Give the preparation type.
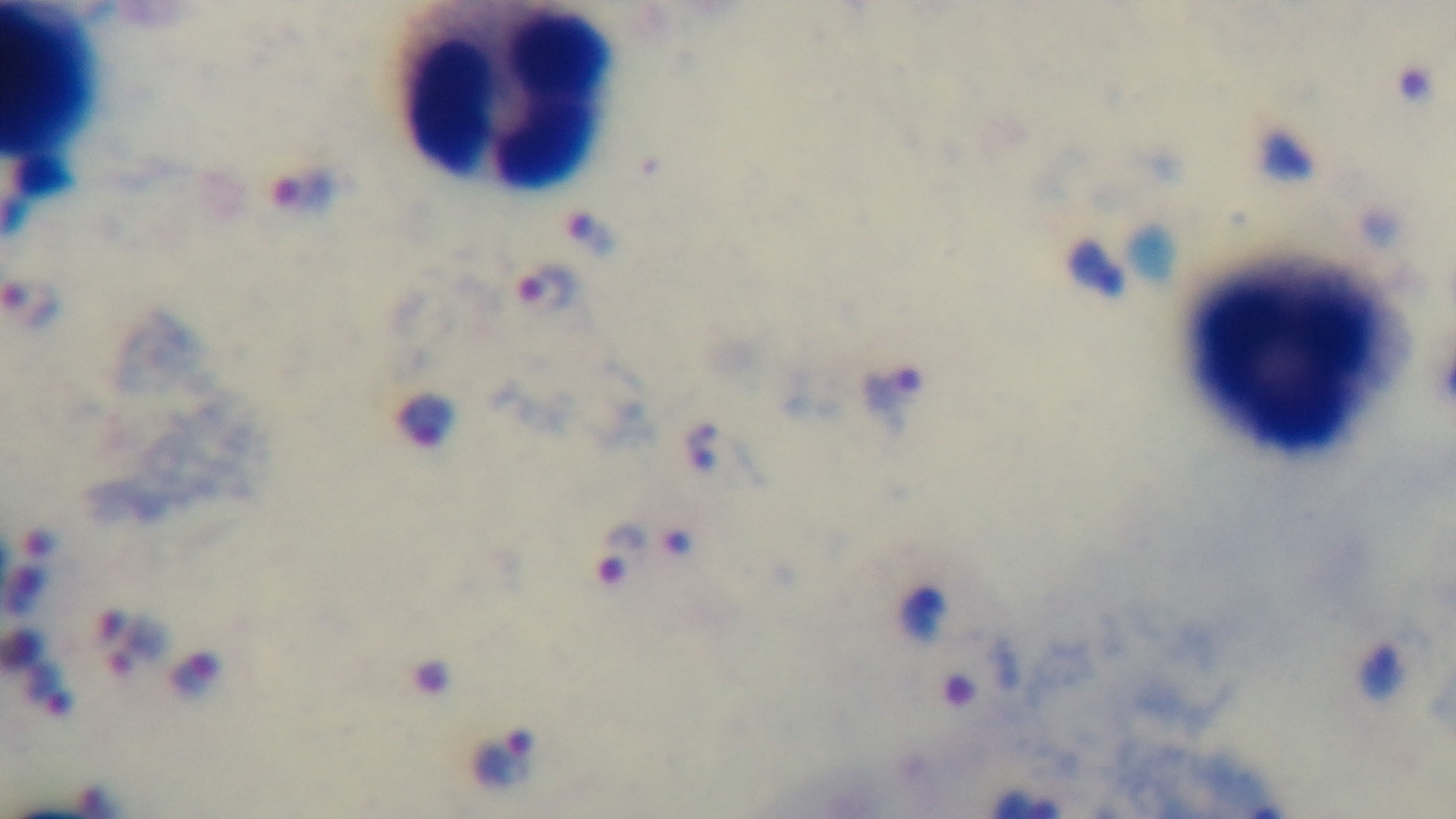

It is a thick blood film.

Mounted 4K digital camera. Giemsa-stained. Single field of view. Photomicrograph. Malaria status: positive. 100x oil-immersion objective.